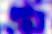
Photomicrograph. Captured at 400x magnification. A leukocyte is seen.